Assess this cell for malaria.
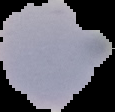
Uninfected.

preparation = thin blood film
image type = segmented cell region on a black background
image size = 115×112 pixels